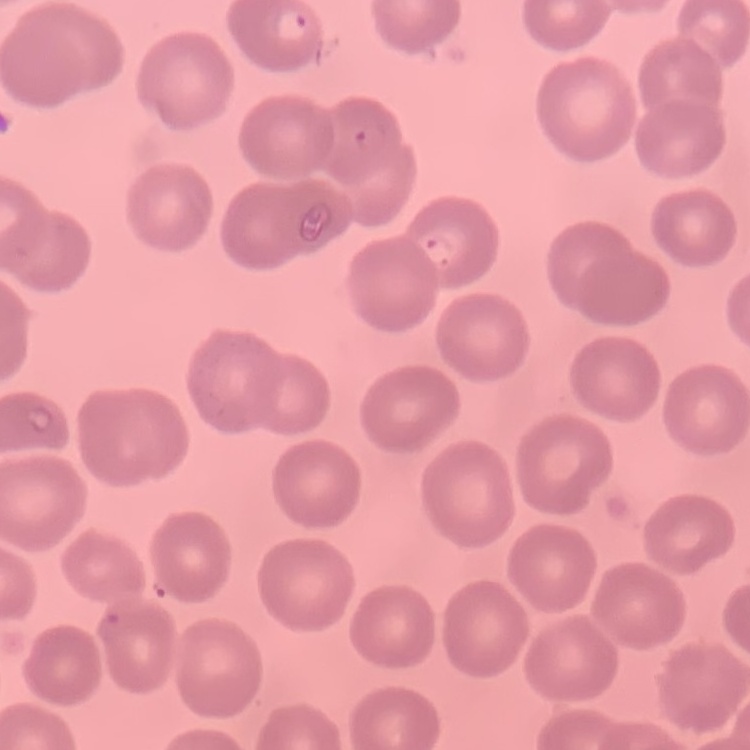

erythrocyte morphology = no rouleaux formation
image type = one tile cut from a larger photomicrograph
stain = Field's or Giemsa
preparation = thin blood smear